Point out every Plasmodium parasite.
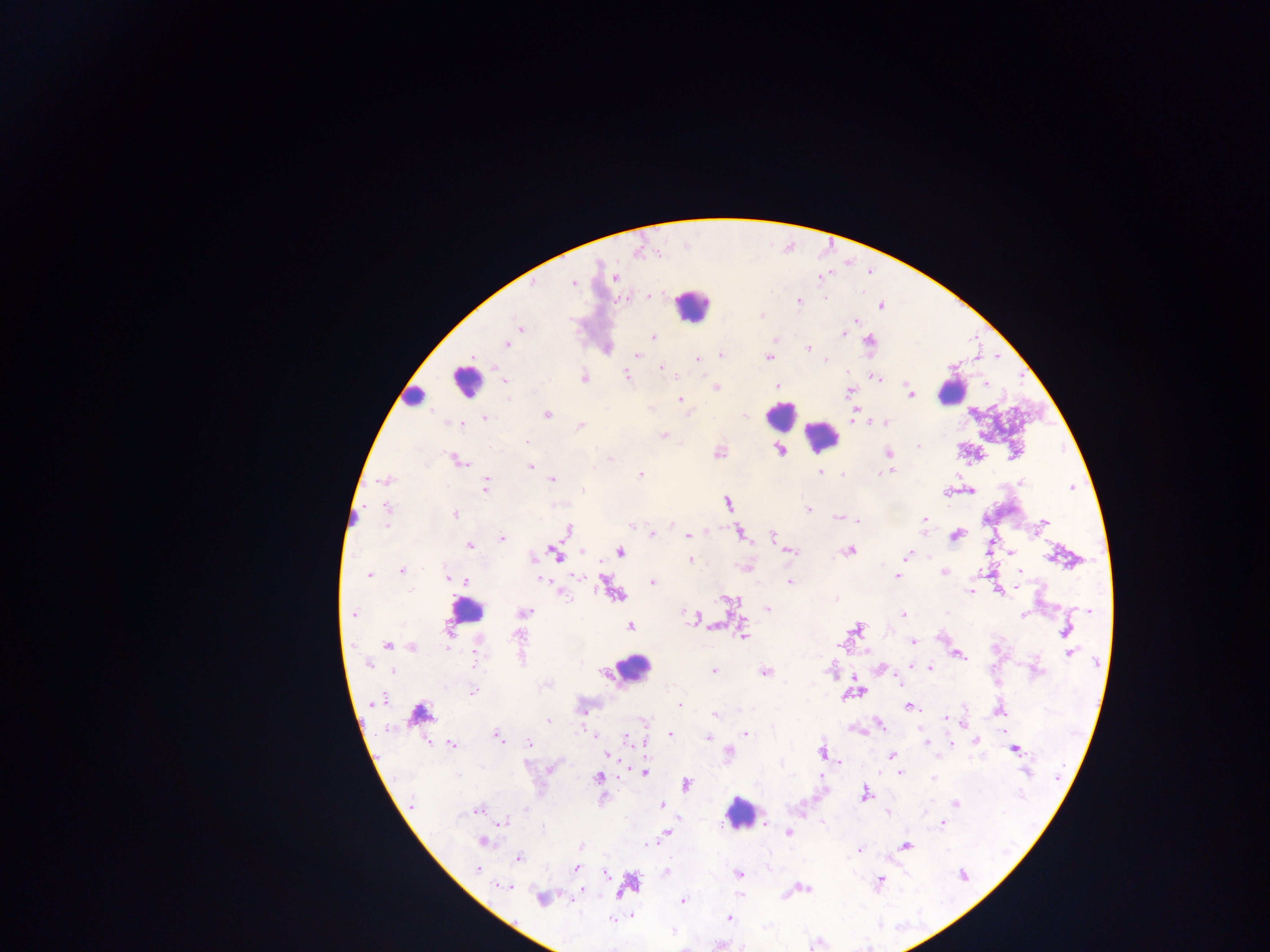
Approximate centers as x y in pixels.
Plasmodium parasites: 614 278; 573 283; 648 296; 624 298; 826 299; 798 302; 854 322; 519 328; 844 336; 655 337; 509 345; 806 348; 638 355; 695 358; 769 358; 826 361; 663 368; 626 374; 584 376; 875 378; 505 381; 778 384; 718 386; 910 395; 679 399; 652 408; 855 408; 744 415; 486 417; 547 417; 447 422; 886 422; 870 423; 464 425; 581 425; 662 434; 916 445; 780 450; 889 452; 718 454; 458 459; 531 468; 892 471; 820 472; 883 472; 639 473; 824 473; 843 475; 552 480; 385 481; 1021 482; 486 485; 1071 487; 972 492; 948 494; 727 502; 383 506; 809 510; 455 514; 837 518; 859 520; 925 520; 1043 522; 670 523; 923 523; 384 527; 631 527; 567 530; 739 531; 653 535; 772 535; 688 536; 956 536; 502 537; 469 545; 621 550; 850 550; 791 552; 1010 553; 556 555; 909 556; 1049 560; 689 561; 402 570; 1018 572; 944 573; 979 573; 369 576; 447 576; 576 576; 897 577; 465 582; 789 582; 606 583; 654 584; 969 592; 998 593; 561 595; 732 601; 768 607; 527 611; 1090 612; 349 615; 902 615; 1022 615; 691 617; 450 618; 624 621; 717 627; 743 627; 858 628; 1064 629; 743 638; 914 642; 387 646; 841 646; 412 648; 1069 654; 958 655; 368 662; 911 665; 880 669; 930 669; 392 671; 713 671; 764 672; 602 673; 900 685; 473 690; 861 693; 846 694; 380 699; 678 705; 908 708; 715 715; 945 718; 948 719; 549 721; 882 725; 965 725; 387 727; 588 732; 858 732; 594 734; 747 735; 670 736; 707 738; 627 739; 500 740; 952 740; 925 741; 975 741; 527 743; 451 744; 1015 750; 646 753; 729 753; 821 754; 607 755; 891 755; 1029 771; 645 773; 900 774; 598 778; 932 779; 688 784; 865 792; 868 796; 661 804; 955 804; 478 809; 888 815; 504 822; 941 823; 789 833; 482 841; 656 841; 581 845; 907 847; 860 850; 518 860; 575 868; 737 874; 605 875; 880 881; 621 893; 540 900; 575 900; 684 900; 632 916; 727 917; 672 932.

Leukocyte locations: 693 301; 460 384; 952 397; 413 401; 775 421; 822 435; 476 616; 634 669; 740 815. Photographed through a microscope with a mobile-phone camera. Collected in Ghana. Single field of view. Thick blood smear. Image is 1270×952 pixels.